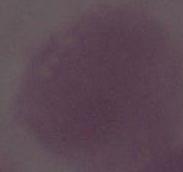
{
  "magnification": "1000x",
  "identification": "red blood cell",
  "modality": "photomicrograph"
}